Locate every Plasmodium vivax-infected red blood cell.
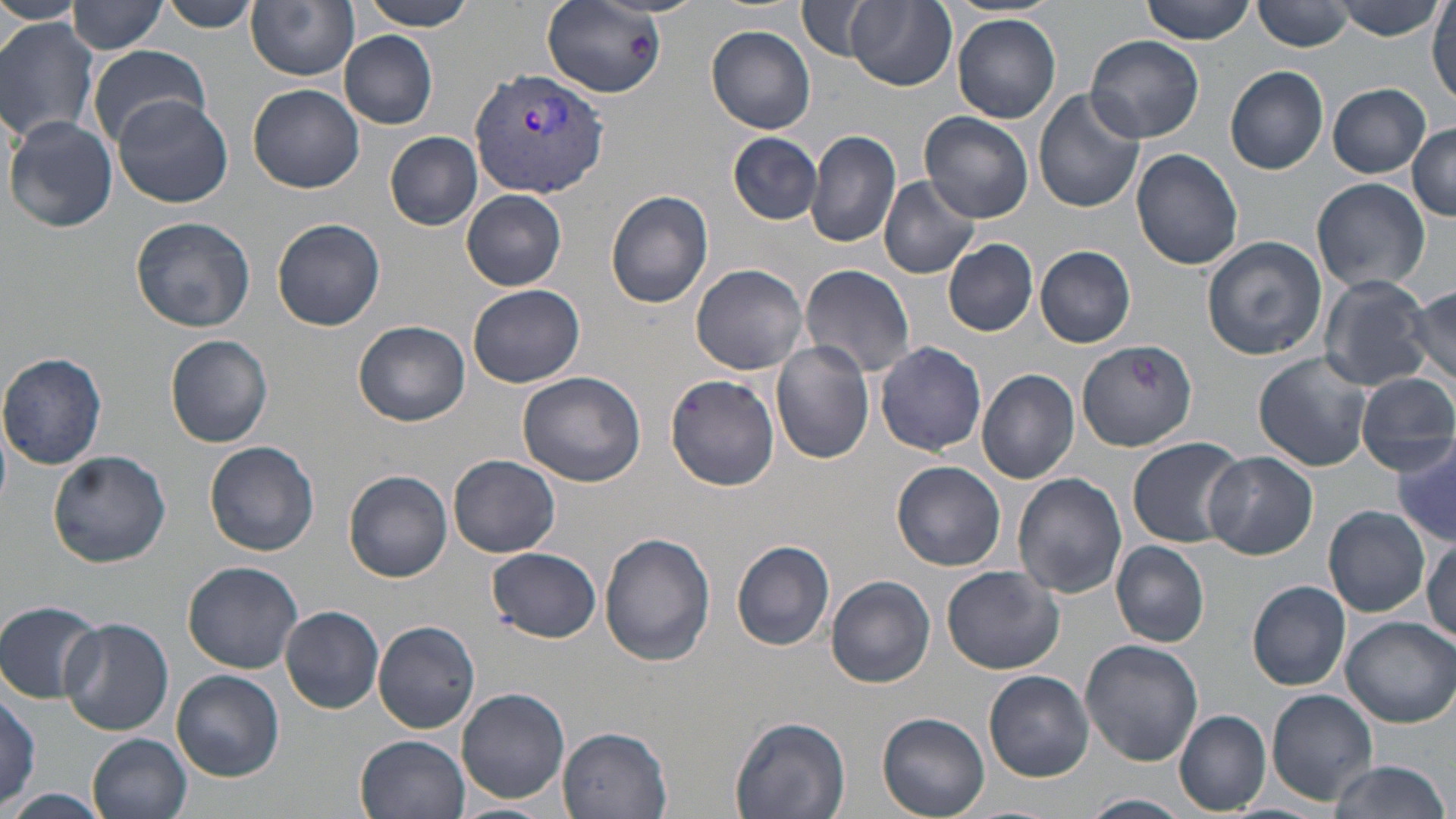

Approximate bounding boxes as [x1, y1, x2, y2] in pixels.
Plasmodium vivax-infected red blood cells: [469, 65, 609, 201].

Summary:
  - Uninfected red blood cell locations: [0, 0, 81, 25], [153, 0, 263, 32], [247, 0, 357, 81], [360, 0, 478, 30], [1139, 0, 1256, 45], [1337, 0, 1444, 38], [68, 1, 168, 55], [798, 1, 878, 61], [1254, 1, 1354, 52], [846, 2, 956, 91], [1429, 3, 1455, 105], [544, 4, 663, 98], [951, 15, 1060, 124], [0, 18, 100, 142], [707, 26, 818, 135], [340, 32, 438, 130], [1084, 33, 1203, 144], [87, 45, 212, 145], [1225, 65, 1329, 175], [1328, 83, 1431, 177], [247, 84, 365, 193], [1034, 88, 1144, 213], [112, 95, 235, 208], [921, 112, 1033, 222], [5, 117, 117, 233], [1408, 124, 1456, 219], [805, 131, 902, 249], [386, 132, 481, 229], [729, 132, 823, 225], [1131, 148, 1244, 270], [878, 176, 981, 279], [1312, 177, 1431, 294], [605, 189, 715, 308], [462, 190, 569, 291], [129, 217, 254, 331], [271, 217, 386, 332], [1201, 235, 1327, 360], [943, 238, 1039, 336], [1035, 246, 1136, 348], [691, 263, 809, 376], [799, 263, 916, 380], [1317, 274, 1430, 391], [468, 285, 585, 389], [1408, 288, 1455, 386], [354, 320, 471, 426], [165, 334, 274, 447], [1076, 339, 1198, 453], [771, 340, 877, 464], [874, 340, 989, 457], [1252, 352, 1375, 473], [0, 353, 107, 469], [976, 367, 1079, 485], [517, 371, 647, 487], [665, 373, 781, 492], [1354, 373, 1456, 474], [1126, 436, 1245, 548], [1392, 439, 1456, 547], [204, 441, 321, 556], [48, 449, 171, 568], [1203, 451, 1317, 559], [448, 454, 561, 558], [891, 461, 1005, 571], [344, 470, 453, 582], [1012, 472, 1127, 599], [1323, 505, 1430, 616], [599, 530, 718, 665], [1423, 536, 1456, 649], [732, 541, 835, 651], [1112, 541, 1209, 647], [488, 549, 602, 642], [184, 561, 301, 673], [943, 566, 1064, 674], [824, 574, 936, 688], [1247, 581, 1352, 691], [1, 600, 105, 701], [280, 605, 385, 713], [60, 617, 173, 735], [1337, 617, 1456, 728], [373, 620, 480, 733], [1080, 638, 1203, 767], [172, 670, 285, 780], [985, 670, 1095, 782], [2, 687, 42, 811], [457, 687, 570, 805], [1266, 690, 1377, 802], [1174, 710, 1271, 814], [877, 711, 992, 817], [730, 716, 852, 819], [558, 727, 674, 817], [90, 733, 192, 819], [355, 734, 469, 819], [1329, 759, 1451, 818], [2, 790, 114, 819], [1083, 793, 1191, 818], [446, 802, 556, 819]
  - Slide-level diagnosis: Plasmodium vivax
  - Field of view: single
  - Modality: light microscopy
  - Magnification: 1000x
  - Image size: 1456×819 pixels
  - Stain: May-Grünwald-Giemsa
  - Preparation: thin blood film